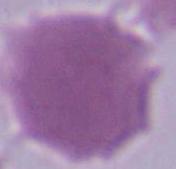

{
  "magnification": "1000x",
  "identification": "erythrocyte",
  "modality": "micrograph"
}